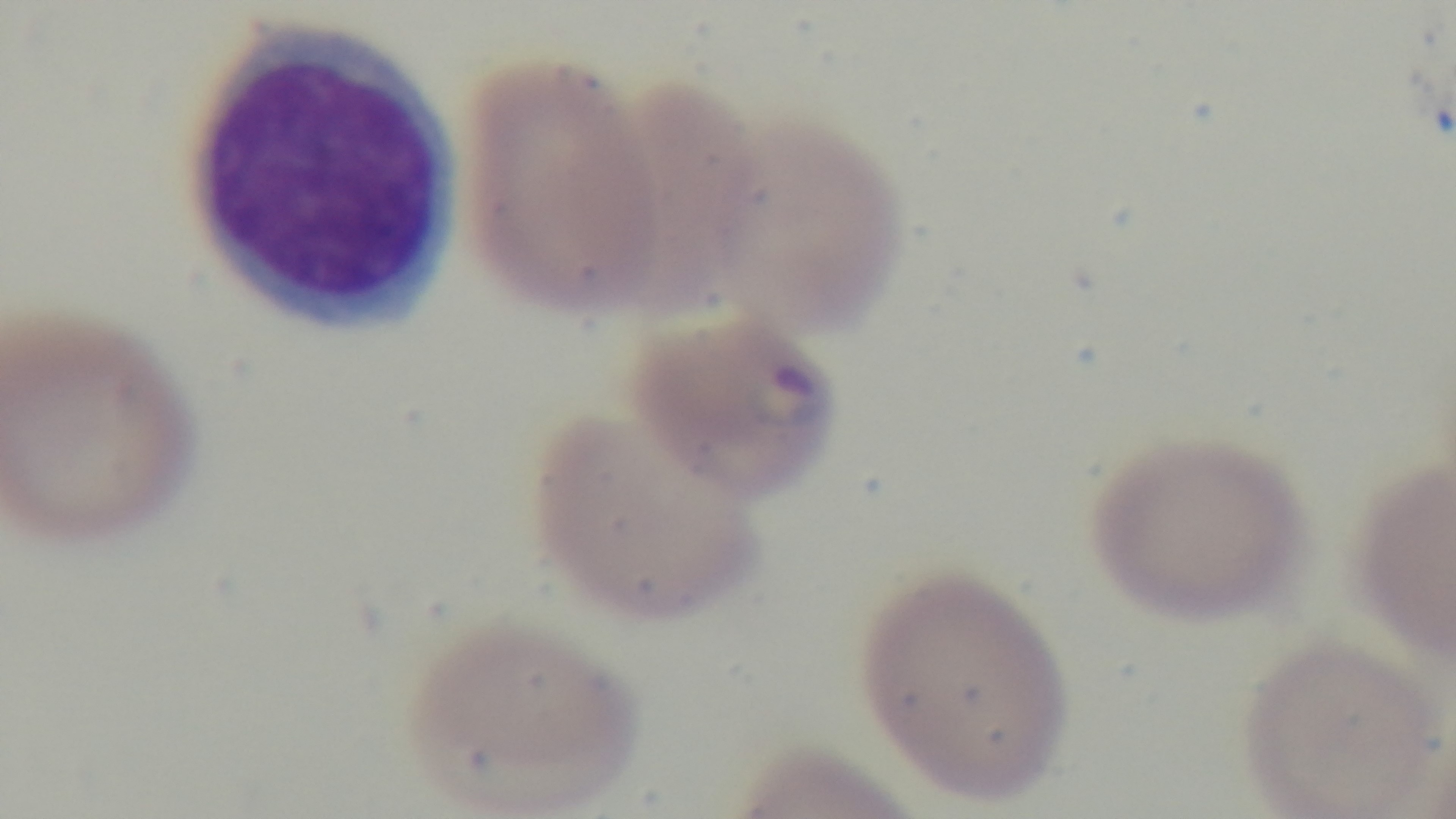
{
  "field_of_view": "one from the slide",
  "stain": "Giemsa",
  "capture": "mounted 4K digital camera",
  "malaria_status": "positive",
  "modality": "light microscopy",
  "preparation": "thin",
  "objective": "100x oil immersion"
}